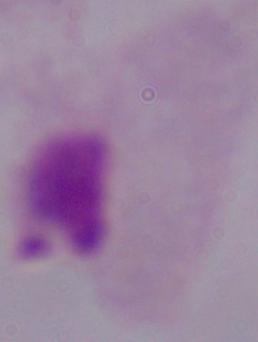
{
  "modality": "micrograph",
  "identification": "trichomonad",
  "magnification": "1000x"
}